Identify the blood parasite species.
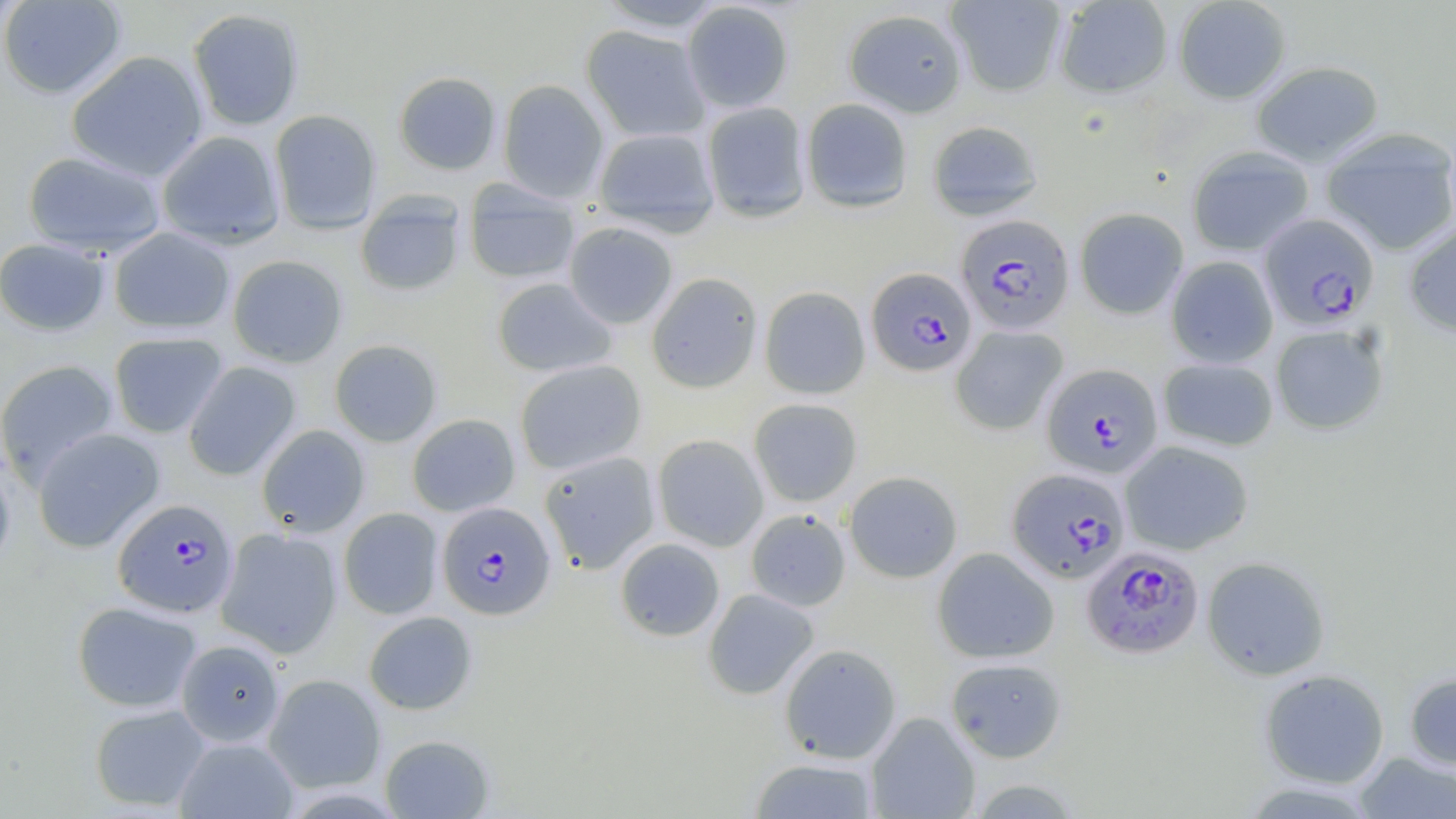
Plasmodium falciparum.

Approximate bounding boxes as named x1/y1/x2/y2 corners in pixels. Uninfected red blood cell locations: (x1=0, y1=0, x2=127, y2=99), (x1=946, y1=0, x2=1067, y2=97), (x1=1053, y1=0, x2=1173, y2=98), (x1=1173, y1=0, x2=1292, y2=104), (x1=594, y1=1, x2=729, y2=33), (x1=681, y1=1, x2=794, y2=113), (x1=187, y1=8, x2=305, y2=131), (x1=843, y1=8, x2=967, y2=118), (x1=581, y1=25, x2=711, y2=142), (x1=65, y1=50, x2=209, y2=182), (x1=1250, y1=60, x2=1384, y2=167), (x1=393, y1=71, x2=501, y2=175), (x1=497, y1=79, x2=609, y2=202), (x1=801, y1=98, x2=914, y2=213), (x1=701, y1=102, x2=812, y2=223), (x1=269, y1=109, x2=382, y2=234), (x1=926, y1=120, x2=1044, y2=221), (x1=593, y1=127, x2=720, y2=236), (x1=1320, y1=128, x2=1456, y2=256), (x1=156, y1=130, x2=286, y2=249), (x1=1187, y1=146, x2=1314, y2=257), (x1=22, y1=150, x2=167, y2=258), (x1=463, y1=180, x2=581, y2=285), (x1=354, y1=192, x2=467, y2=297), (x1=1074, y1=207, x2=1189, y2=320), (x1=564, y1=222, x2=678, y2=329), (x1=1403, y1=222, x2=1456, y2=337), (x1=108, y1=227, x2=235, y2=334), (x1=0, y1=237, x2=111, y2=336), (x1=227, y1=254, x2=348, y2=368), (x1=1166, y1=255, x2=1278, y2=368), (x1=646, y1=272, x2=763, y2=393), (x1=491, y1=277, x2=617, y2=378), (x1=759, y1=286, x2=870, y2=399), (x1=1270, y1=323, x2=1390, y2=435), (x1=950, y1=325, x2=1067, y2=435), (x1=109, y1=332, x2=228, y2=438), (x1=329, y1=339, x2=443, y2=447), (x1=1158, y1=358, x2=1278, y2=451), (x1=0, y1=359, x2=119, y2=486), (x1=515, y1=359, x2=647, y2=475), (x1=183, y1=361, x2=302, y2=480), (x1=748, y1=398, x2=862, y2=507), (x1=407, y1=414, x2=520, y2=517), (x1=256, y1=424, x2=370, y2=537), (x1=31, y1=427, x2=166, y2=553), (x1=652, y1=434, x2=769, y2=551), (x1=1120, y1=440, x2=1254, y2=555), (x1=539, y1=450, x2=660, y2=574), (x1=0, y1=458, x2=16, y2=578), (x1=844, y1=471, x2=962, y2=583), (x1=339, y1=508, x2=443, y2=619), (x1=745, y1=509, x2=851, y2=612), (x1=215, y1=528, x2=343, y2=658), (x1=614, y1=538, x2=725, y2=642), (x1=932, y1=547, x2=1059, y2=663), (x1=1202, y1=555, x2=1331, y2=681), (x1=703, y1=588, x2=820, y2=700), (x1=72, y1=600, x2=202, y2=713), (x1=363, y1=611, x2=478, y2=715), (x1=176, y1=639, x2=285, y2=747), (x1=779, y1=643, x2=901, y2=764), (x1=945, y1=657, x2=1067, y2=763), (x1=1259, y1=669, x2=1390, y2=788), (x1=1404, y1=671, x2=1456, y2=771), (x1=264, y1=673, x2=386, y2=793), (x1=89, y1=703, x2=212, y2=812), (x1=866, y1=711, x2=980, y2=818), (x1=379, y1=734, x2=495, y2=818), (x1=174, y1=737, x2=299, y2=819), (x1=1355, y1=751, x2=1455, y2=819), (x1=748, y1=757, x2=879, y2=818). Plasmodium falciparum-infected red blood cell locations: (x1=1259, y1=212, x2=1380, y2=331), (x1=956, y1=214, x2=1075, y2=334), (x1=866, y1=267, x2=977, y2=376), (x1=1042, y1=364, x2=1164, y2=478), (x1=1007, y1=467, x2=1131, y2=583), (x1=113, y1=498, x2=239, y2=618), (x1=436, y1=501, x2=556, y2=620), (x1=1082, y1=546, x2=1204, y2=659). Image is 1456×819 pixels. 1000x magnification. Single field of view. Optical microscopy. Thin blood smear. May-Grünwald-Giemsa stain.